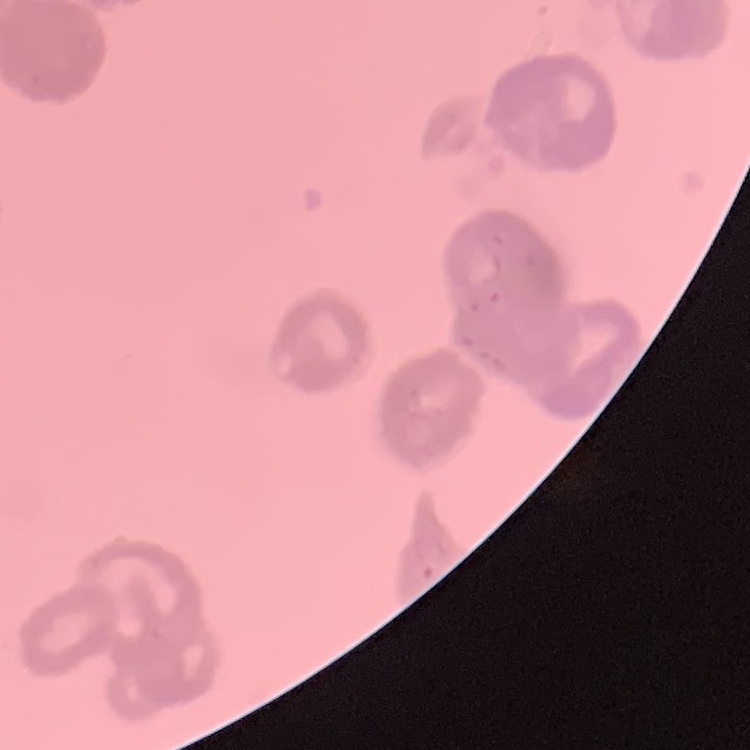 The red blood cells show rouleaux formation. Square crop of a larger photomicrograph. Field's or Giemsa stain. Thin blood film.